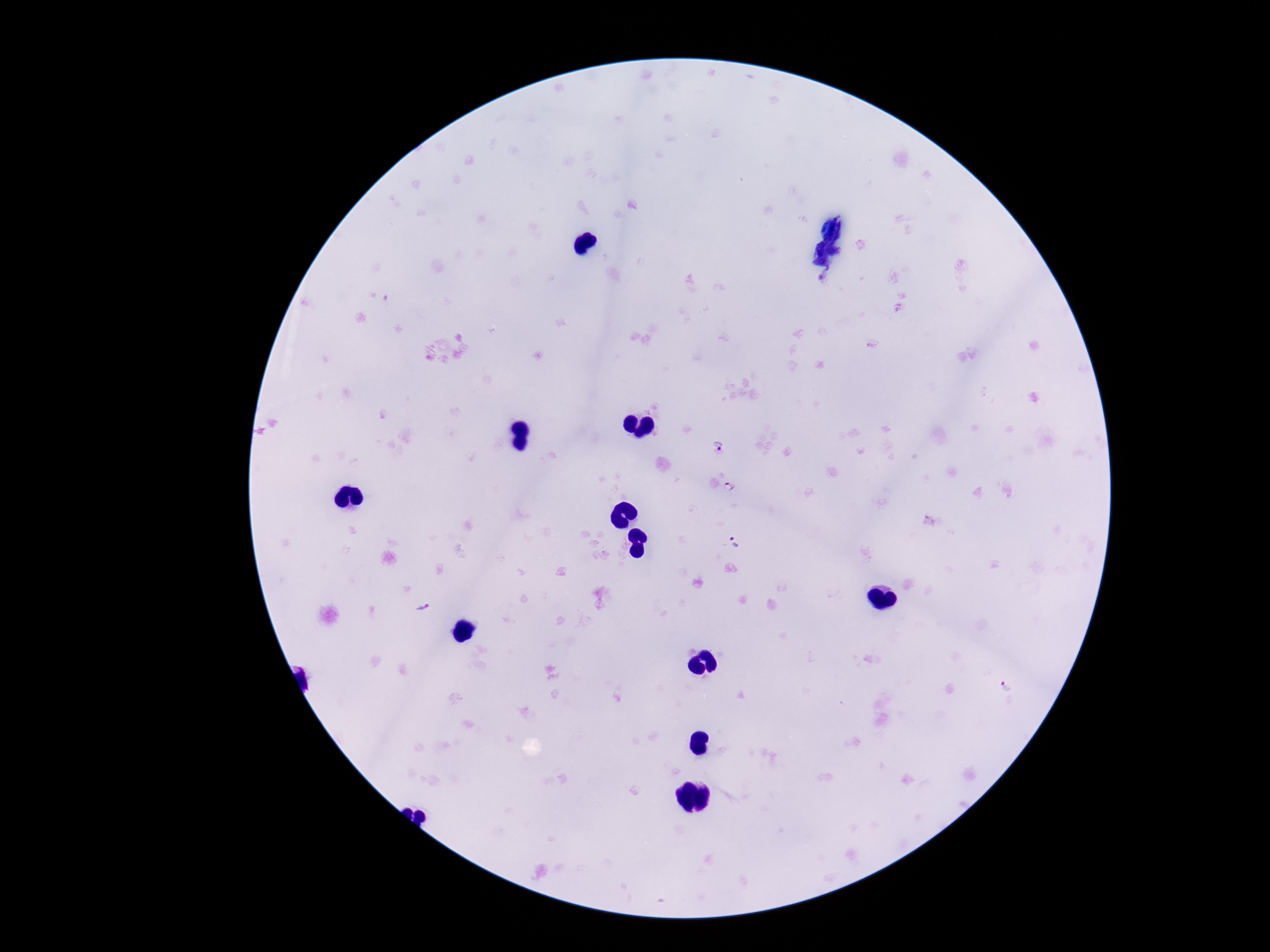
Approximate centers as {x, y} in pixels. Plasmodium parasite locations: {718, 446}, {727, 487}, {736, 543}, {422, 609}, {1007, 686}. 100x magnification. Giemsa-stained preparation. One field from this slide. Smartphone photograph taken through the microscope eyepiece. Patient malaria status: infected. Thick blood smear. Image is 1270×952 pixels.